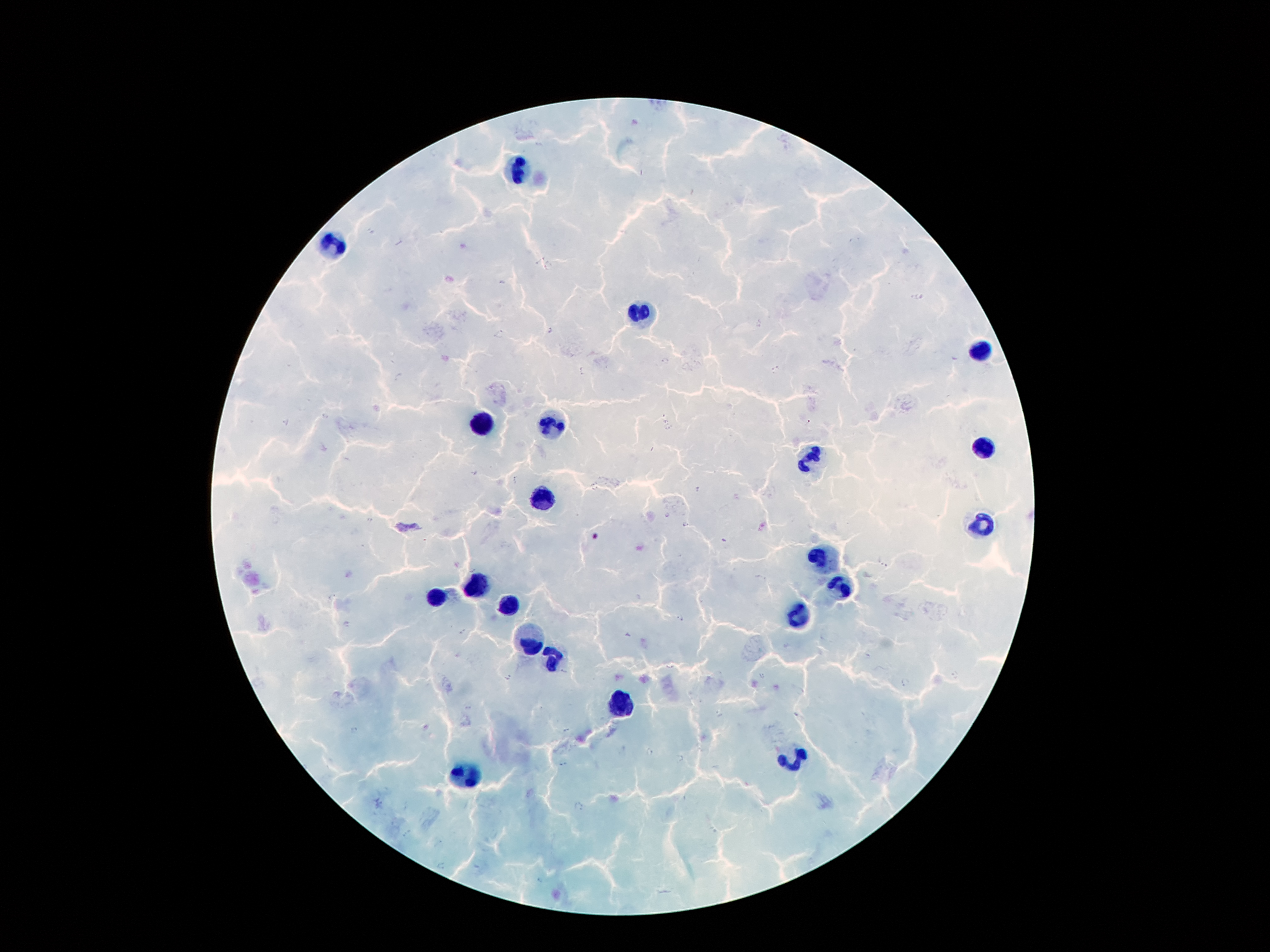
coordinate format = approximate centers as (x, y) in pixels
leukocyte locations = (521, 168), (332, 246), (641, 313), (981, 348), (550, 422), (483, 426), (983, 445), (809, 458), (544, 497), (981, 523), (819, 560), (477, 584), (844, 584), (435, 598), (506, 607), (800, 615), (533, 638), (552, 661), (615, 703), (792, 758), (466, 775)
malaria parasite locations = (398, 241), (538, 259), (549, 267), (549, 330), (501, 334), (663, 361), (778, 368), (581, 371), (324, 416), (287, 422), (809, 422), (514, 480), (666, 515), (685, 526), (882, 566), (333, 596), (681, 618), (347, 624), (462, 632), (564, 672), (762, 676), (507, 677), (355, 731), (566, 731), (648, 753), (562, 765), (578, 807), (408, 833), (441, 865)
field of view = one from this slide
preparation = thick peripheral-blood smear
patient malaria status = infected with Plasmodium falciparum
capture = smartphone through the microscope eyepiece
stain = Giemsa
magnification = 100x
image size = 1270×952 pixels